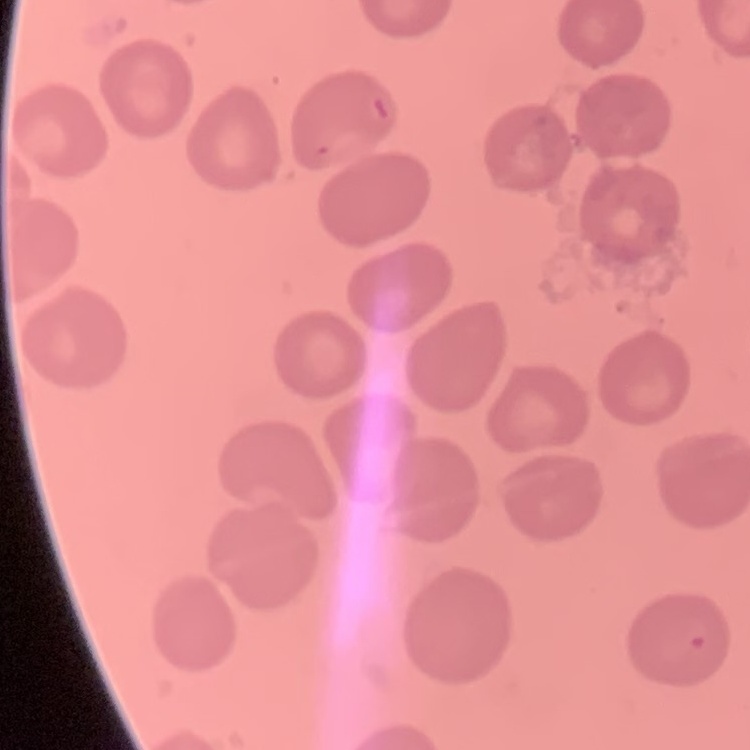

Summary:
  - Red blood cell morphology: no rouleaux formation
  - Preparation: thin blood film
  - Stain: Field's or Giemsa
  - Image type: square crop of a larger photomicrograph